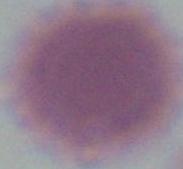

Captured at 1000x magnification. An erythrocyte is shown. Micrograph.